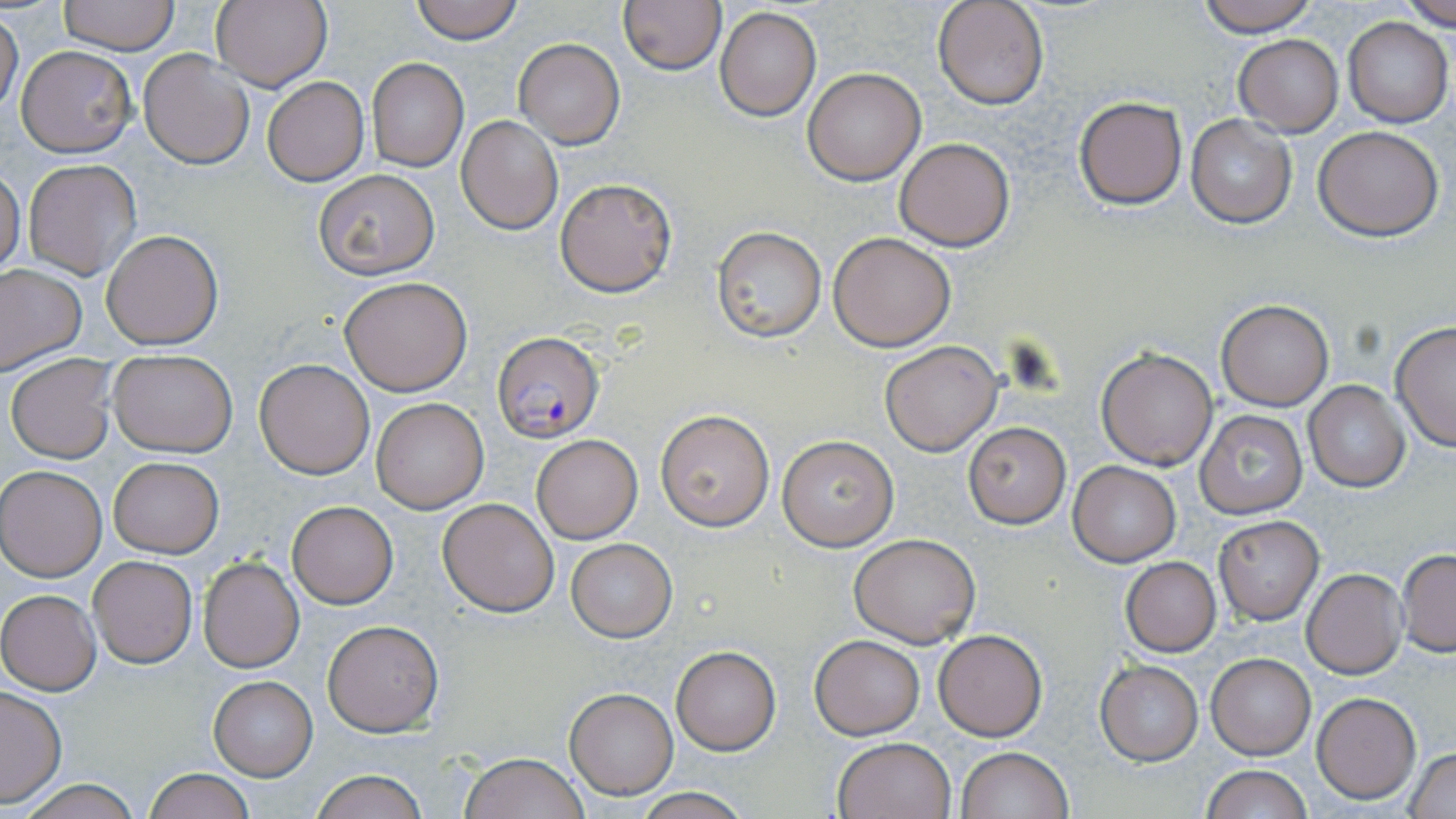
Approximate bounding boxes as [x1, y1, x2, y2] in pixels. Plasmodium falciparum-infected red blood cell locations: [491, 331, 603, 442]. Uninfected red blood cell locations: [57, 0, 179, 53], [409, 0, 526, 44], [616, 0, 725, 74], [932, 0, 1049, 110], [1197, 0, 1320, 37], [1397, 0, 1456, 29], [211, 1, 332, 90], [715, 7, 821, 121], [0, 12, 23, 115], [1341, 17, 1453, 127], [1233, 34, 1342, 136], [515, 39, 624, 149], [16, 46, 136, 156], [136, 48, 254, 170], [367, 58, 468, 171], [803, 66, 927, 185], [262, 76, 369, 186], [1074, 97, 1187, 210], [1185, 114, 1297, 230], [457, 115, 563, 235], [1314, 126, 1443, 241], [894, 137, 1016, 251], [22, 159, 142, 281], [0, 167, 24, 277], [313, 170, 440, 278], [554, 176, 678, 298], [711, 226, 826, 344], [102, 229, 222, 349], [829, 232, 956, 351], [0, 263, 86, 375], [340, 276, 472, 395], [1216, 300, 1333, 410], [1389, 321, 1456, 453], [879, 340, 1002, 455], [1097, 347, 1218, 469], [108, 350, 237, 457], [6, 354, 118, 463], [254, 358, 376, 479], [1302, 380, 1410, 493], [370, 396, 490, 514], [655, 409, 776, 530], [1193, 410, 1306, 519], [961, 422, 1071, 528], [531, 433, 643, 544], [777, 435, 899, 551], [108, 456, 223, 557], [1067, 461, 1181, 566], [1, 465, 106, 581], [438, 498, 561, 617], [287, 501, 398, 607], [1214, 515, 1324, 624], [849, 532, 981, 647], [567, 539, 676, 641], [1397, 548, 1456, 656], [88, 555, 197, 668], [197, 555, 306, 673], [1120, 557, 1221, 656], [1301, 569, 1407, 679], [0, 589, 101, 695], [322, 619, 444, 736], [932, 629, 1047, 741], [810, 635, 924, 739], [669, 646, 781, 754], [1207, 653, 1314, 760], [1096, 660, 1202, 765], [209, 675, 317, 781], [0, 686, 67, 807], [565, 687, 677, 800], [1312, 692, 1421, 803], [833, 736, 956, 819], [955, 747, 1072, 819], [1407, 747, 1456, 818], [459, 751, 588, 819], [1201, 764, 1310, 819], [144, 768, 254, 819], [309, 770, 431, 818], [14, 777, 143, 818], [627, 791, 757, 819]. Slide-level diagnosis: Plasmodium falciparum. May-Grünwald-Giemsa-stained preparation. Captured at 1000x magnification. Image is 1456×819 pixels. One field of a larger specimen. Thin blood film. Light microscopy.